Locate every Plasmodium malariae-infected red blood cell.
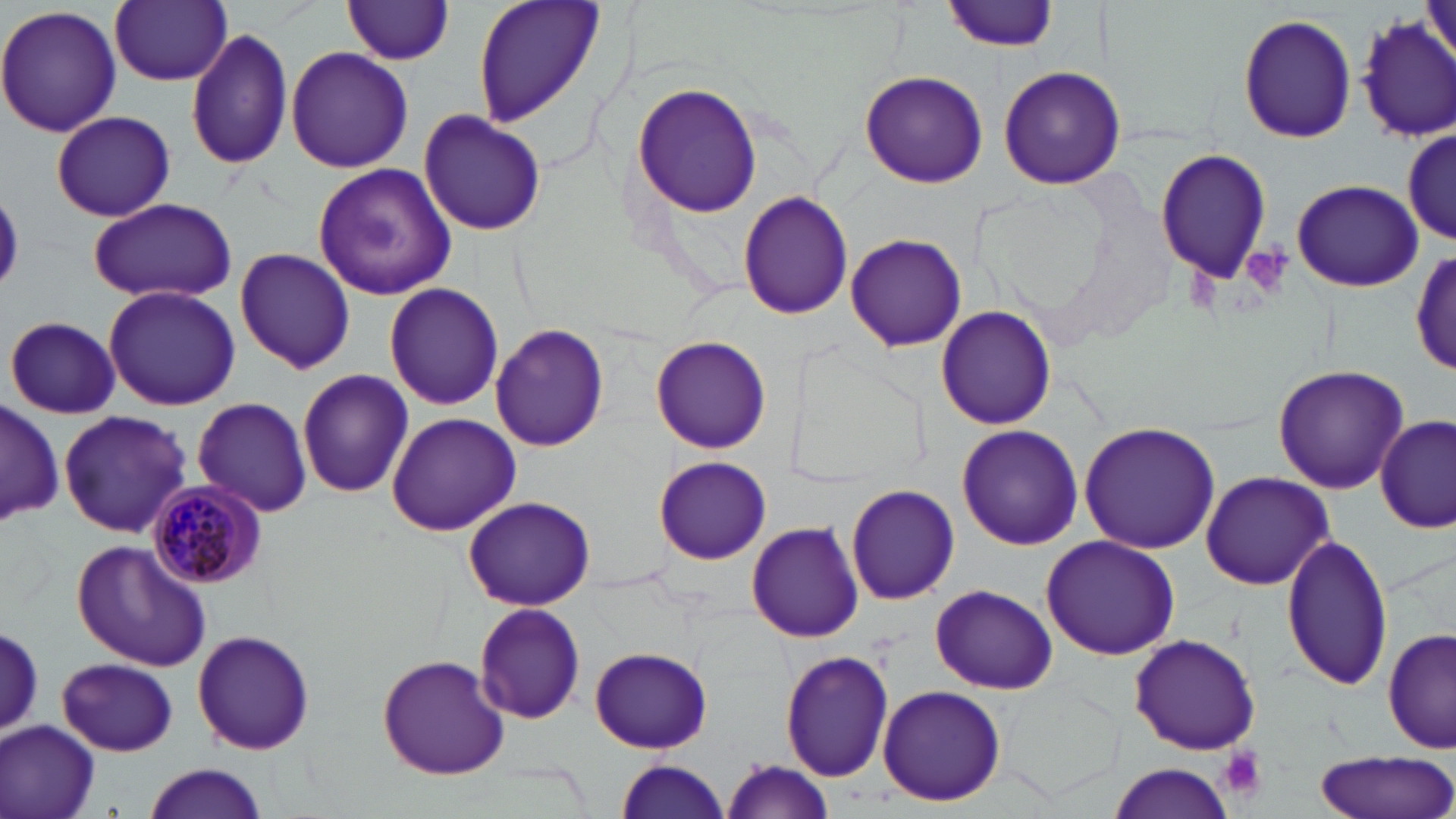

Approximate bounding boxes as [x1, y1, x2, y2] in pixels.
Plasmodium malariae-infected red blood cells: [148, 482, 267, 586].

Platelet locations: [1240, 246, 1293, 298], [1219, 746, 1267, 799]. Uninfected red blood cell locations: [471, 0, 606, 129], [943, 0, 1060, 52], [110, 1, 231, 87], [341, 1, 457, 65], [0, 4, 123, 140], [1354, 11, 1456, 144], [1238, 12, 1356, 144], [185, 26, 294, 170], [284, 45, 414, 174], [996, 65, 1128, 190], [858, 69, 988, 188], [632, 82, 763, 217], [416, 108, 549, 237], [51, 110, 177, 222], [1403, 123, 1453, 246], [1155, 147, 1273, 287], [311, 164, 458, 300], [1290, 178, 1426, 294], [736, 191, 854, 320], [0, 194, 26, 288], [88, 197, 236, 304], [844, 233, 967, 353], [233, 247, 357, 374], [1410, 251, 1455, 374], [383, 283, 505, 411], [103, 284, 240, 412], [935, 305, 1056, 430], [5, 315, 121, 419], [491, 322, 609, 451], [651, 335, 772, 454], [1271, 364, 1407, 494], [296, 369, 414, 499], [191, 395, 314, 518], [2, 398, 61, 527], [58, 410, 192, 538], [386, 413, 520, 537], [1376, 417, 1453, 534], [1078, 422, 1221, 556], [956, 425, 1083, 550], [653, 456, 771, 563], [1199, 471, 1333, 591], [844, 484, 959, 606], [463, 497, 595, 610], [745, 520, 864, 643], [1281, 533, 1394, 692], [1039, 535, 1180, 661], [73, 539, 212, 672], [928, 585, 1057, 693], [474, 602, 586, 724], [1, 625, 44, 735], [1383, 627, 1454, 758], [191, 629, 316, 756], [1128, 633, 1261, 755], [588, 647, 714, 754], [780, 648, 895, 782], [377, 653, 511, 779], [58, 658, 181, 755], [877, 684, 1006, 806], [0, 719, 100, 819], [1312, 749, 1455, 819], [611, 759, 733, 818], [719, 759, 834, 817], [1106, 762, 1237, 818], [141, 764, 269, 819]. Slide-level diagnosis: Plasmodium malariae. May-Grünwald-Giemsa stain. Single field of view. 1000x magnification. Image is 1456×819 pixels. Optical microscopy. Thin blood smear.